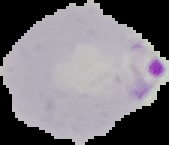

Summary:
  - Image type: cell region segmented out of the field of view; surrounding area masked to black
  - Malaria status: parasitized
  - Image size: 169×145 pixels
  - Preparation: thin blood film